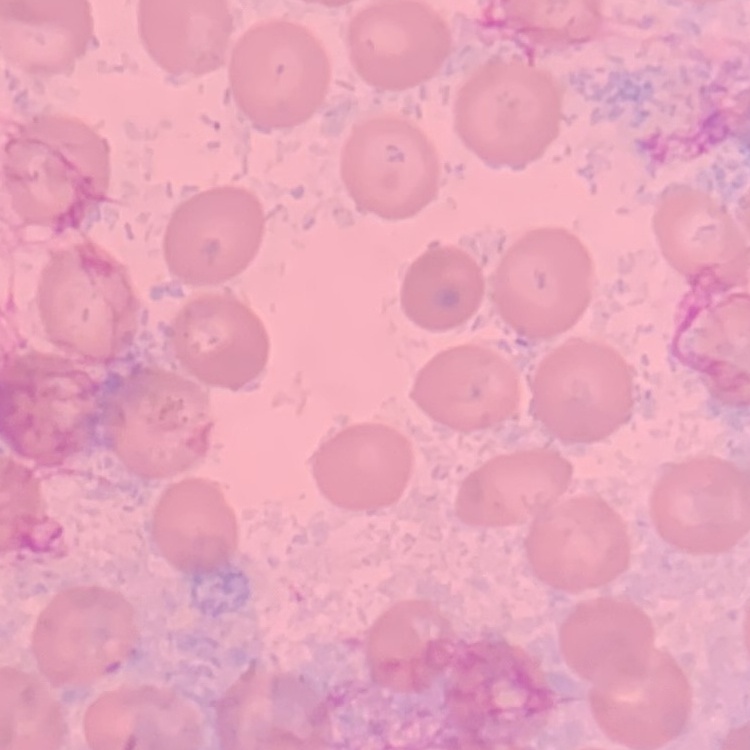
Summary:
  - Erythrocyte morphology: no rouleaux formation
  - Image type: square crop of a larger photomicrograph
  - Preparation: thin blood film
  - Stain: Field's or Giemsa